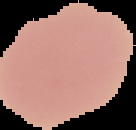
Summary:
  - Image size: 136×130 pixels
  - Preparation: thin blood smear
  - Image type: segmented cell region with the area outside set to black
  - Malaria status: uninfected